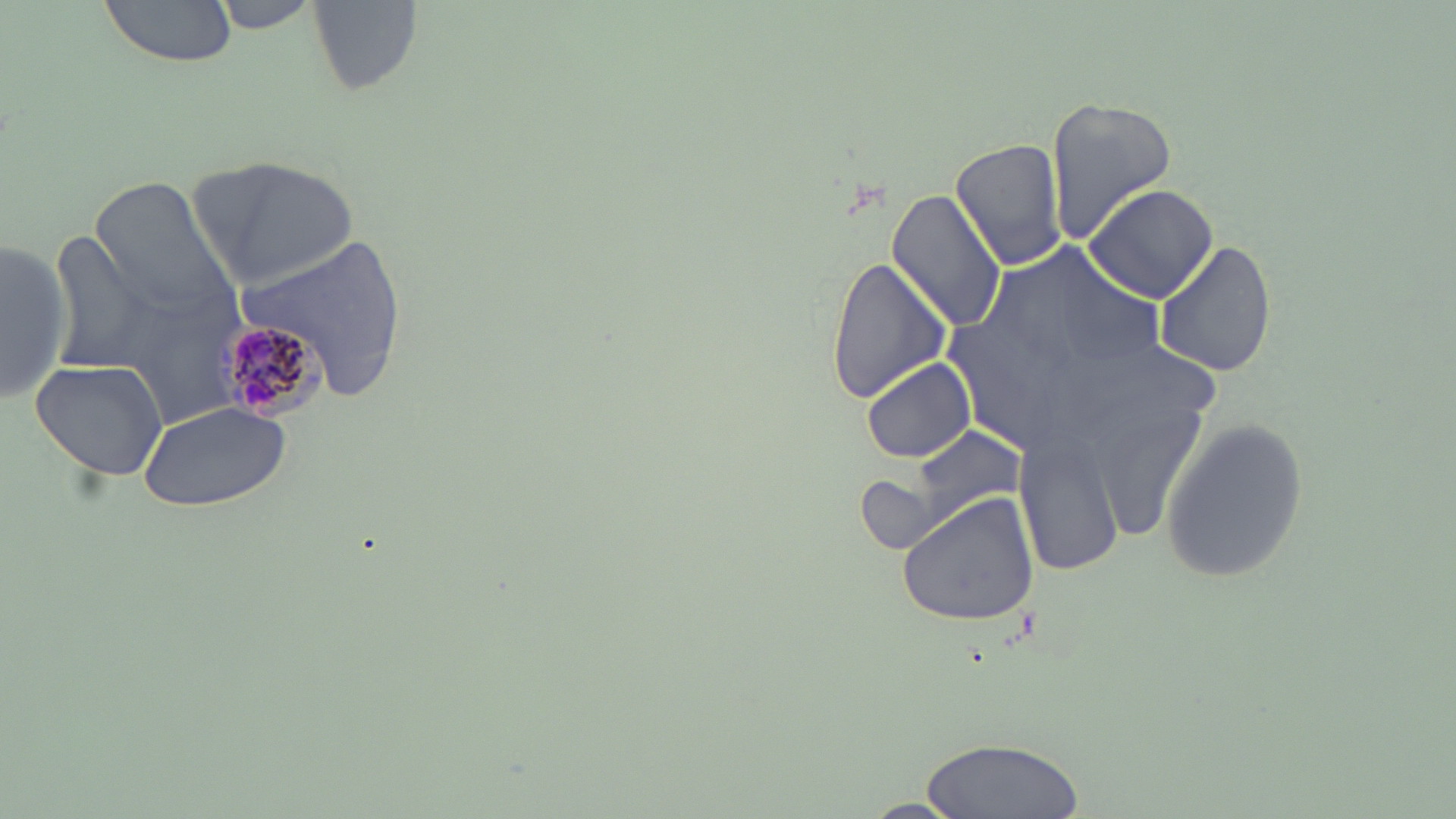
Summary:
  - Coordinate format: approximate bounding boxes as [x1, y1, x2, y2] in pixels
  - Plasmodium malariae-infected red blood cell locations: [210, 316, 328, 421]
  - Uninfected red blood cell locations: [100, 0, 241, 67], [207, 0, 324, 31], [307, 3, 424, 99], [1045, 95, 1178, 239], [951, 138, 1068, 271], [195, 154, 359, 284], [88, 175, 242, 328], [1084, 183, 1217, 301], [886, 188, 1007, 331], [47, 232, 160, 373], [1, 233, 71, 409], [1153, 242, 1277, 377], [824, 255, 951, 405], [861, 355, 977, 464], [29, 357, 170, 482], [137, 400, 294, 514], [1161, 415, 1310, 586], [910, 421, 1025, 522], [1018, 432, 1121, 574], [896, 491, 1038, 627], [919, 733, 1083, 817]
  - Slide-level diagnosis: Plasmodium malariae
  - Image size: 1456×819 pixels
  - Stain: May-Grünwald-Giemsa
  - Preparation: thin blood smear
  - Magnification: 1000x
  - Modality: optical microscopy
  - Field of view: one of a larger specimen